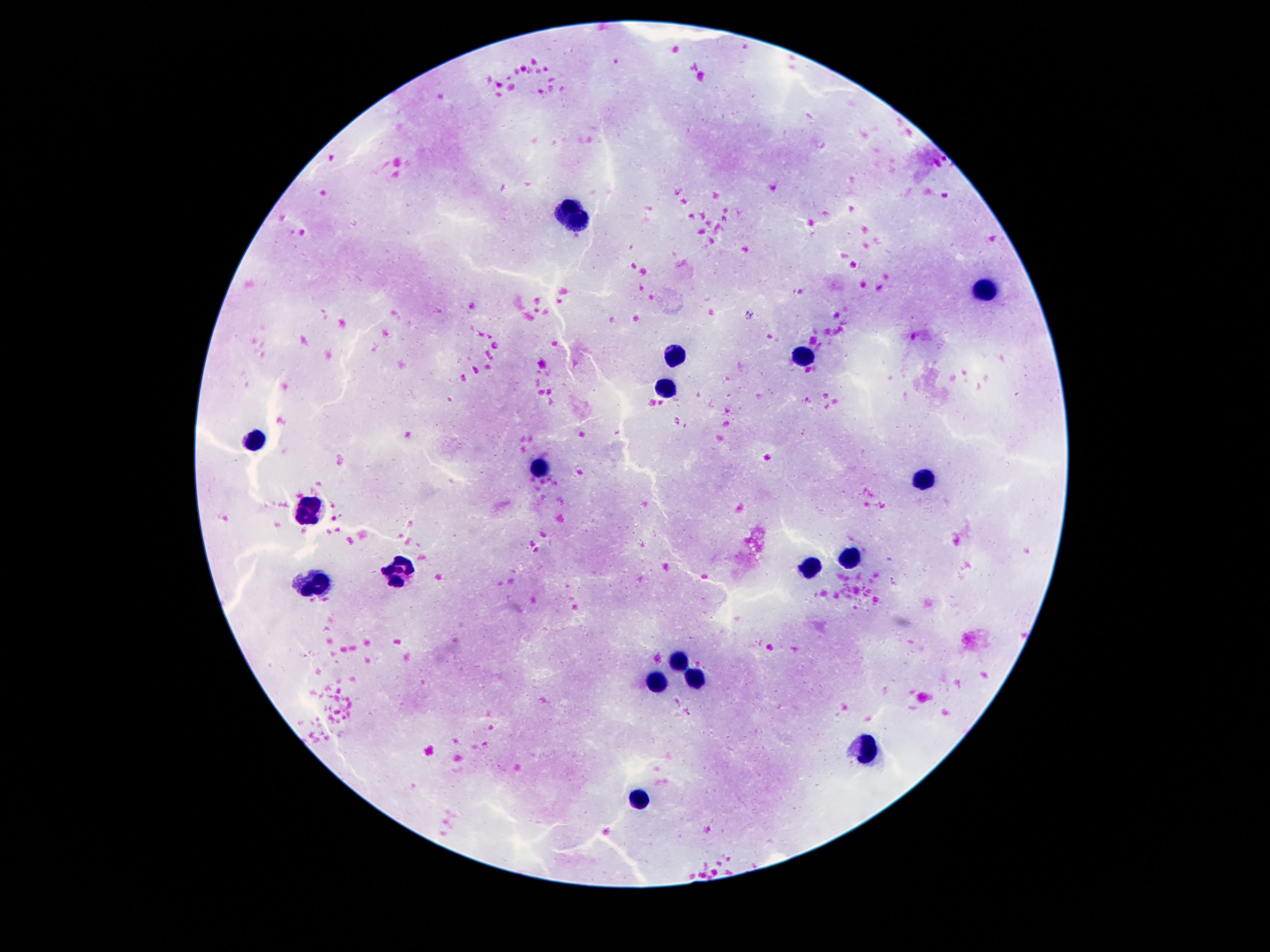

Approximate centers as [x, y] in pixels.
Summary:
  - Leukocyte locations: [575, 215], [983, 291], [800, 355], [673, 356], [663, 389], [257, 437], [538, 473], [925, 479], [312, 507], [852, 558], [809, 568], [398, 571], [314, 584], [678, 660], [698, 678], [657, 683], [871, 749], [641, 797]
  - Patient malaria status: not infected
  - Preparation: thick blood smear
  - Image size: 1270×952 pixels
  - Magnification: 100x
  - Capture: smartphone camera through the microscope eyepiece
  - Field of view: one from this slide
  - Stain: Giemsa